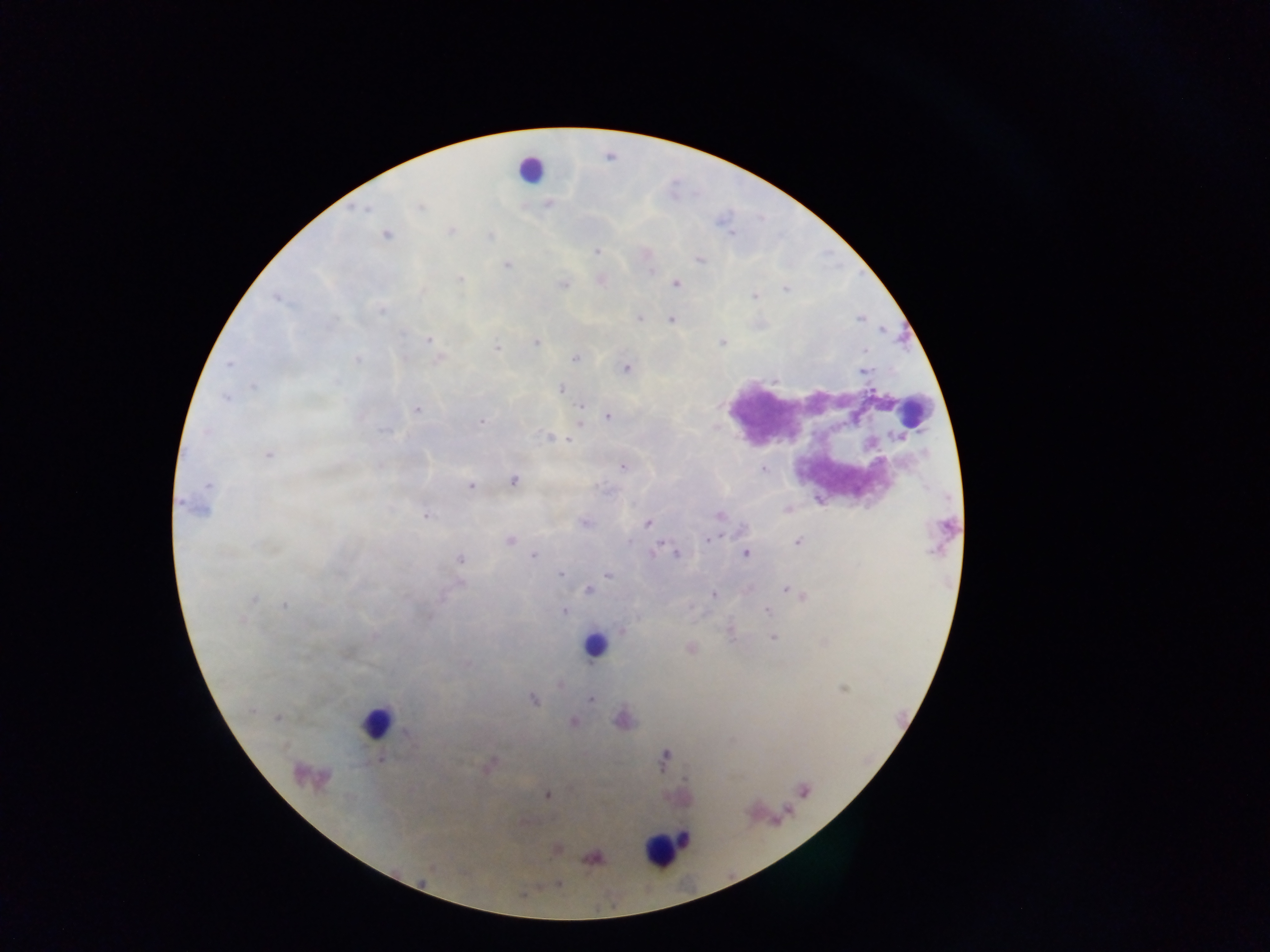
Approximate centers as {x, y} in pixels.
Summary:
  - Leukocyte locations: {530, 168}, {914, 411}, {593, 645}, {376, 722}, {663, 849}
  - Malaria parasite locations: {420, 207}, {363, 209}, {450, 231}, {386, 235}, {597, 252}, {699, 260}, {507, 265}, {651, 271}, {459, 279}, {676, 284}, {563, 285}, {785, 289}, {755, 296}, {277, 299}, {382, 309}, {639, 319}, {671, 319}, {860, 319}, {428, 341}, {536, 342}, {722, 342}, {497, 349}, {864, 350}, {575, 358}, {357, 359}, {229, 364}, {626, 368}, {863, 370}, {774, 380}, {253, 387}, {560, 390}, {226, 398}, {581, 406}, {417, 409}, {608, 417}, {481, 421}, {384, 430}, {207, 432}, {548, 436}, {559, 437}, {568, 440}, {268, 455}, {622, 467}, {764, 469}, {514, 481}, {207, 484}, {470, 486}, {180, 502}, {787, 509}, {425, 515}, {718, 516}, {585, 523}, {647, 523}, {708, 539}, {509, 540}, {630, 541}, {797, 541}, {653, 552}, {745, 553}, {676, 554}, {533, 556}, {460, 558}, {560, 573}, {608, 574}, {785, 588}, {588, 590}, {713, 595}, {802, 596}, {254, 599}, {284, 605}, {767, 611}, {564, 612}, {241, 620}, {622, 631}, {772, 637}, {691, 649}, {842, 689}, {533, 699}, {591, 700}, {252, 710}, {277, 718}, {574, 722}, {408, 734}, {381, 759}, {489, 765}, {548, 795}, {557, 850}, {594, 858}, {559, 884}
  - Preparation: thick blood film
  - Capture: mobile-phone photograph through a microscope
  - Image size: 1270×952 pixels
  - Country: Ghana
  - Field of view: single